Report the malaria status of this cell.
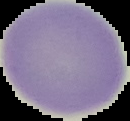
It is uninfected.

Image is 130×121 pixels. Cell region segmented out of the field of view; the surrounding area is masked to black. From a thin blood smear.